Assess this cell for malaria.
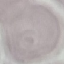
Uninfected.

Thin smear of blood. Cell patch, automatically extracted from a larger field of view and resized to 64 × 64 pixels. Acquired by smartphone through the microscope eyepiece. Giemsa stain.